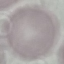 Malaria status: uninfected. Photographed with a smartphone camera at the microscope eyepiece. Thin blood smear. Automatically extracted cell patch, resized to 64 × 64 pixels. Giemsa stain.